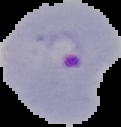 Image is 121×127 pixels. Segmented cell region on a black background. From a thin blood smear. Malaria status: parasitized.